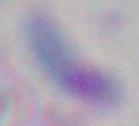
magnification: 1000x
modality: micrograph
identification: Toxoplasma gondii